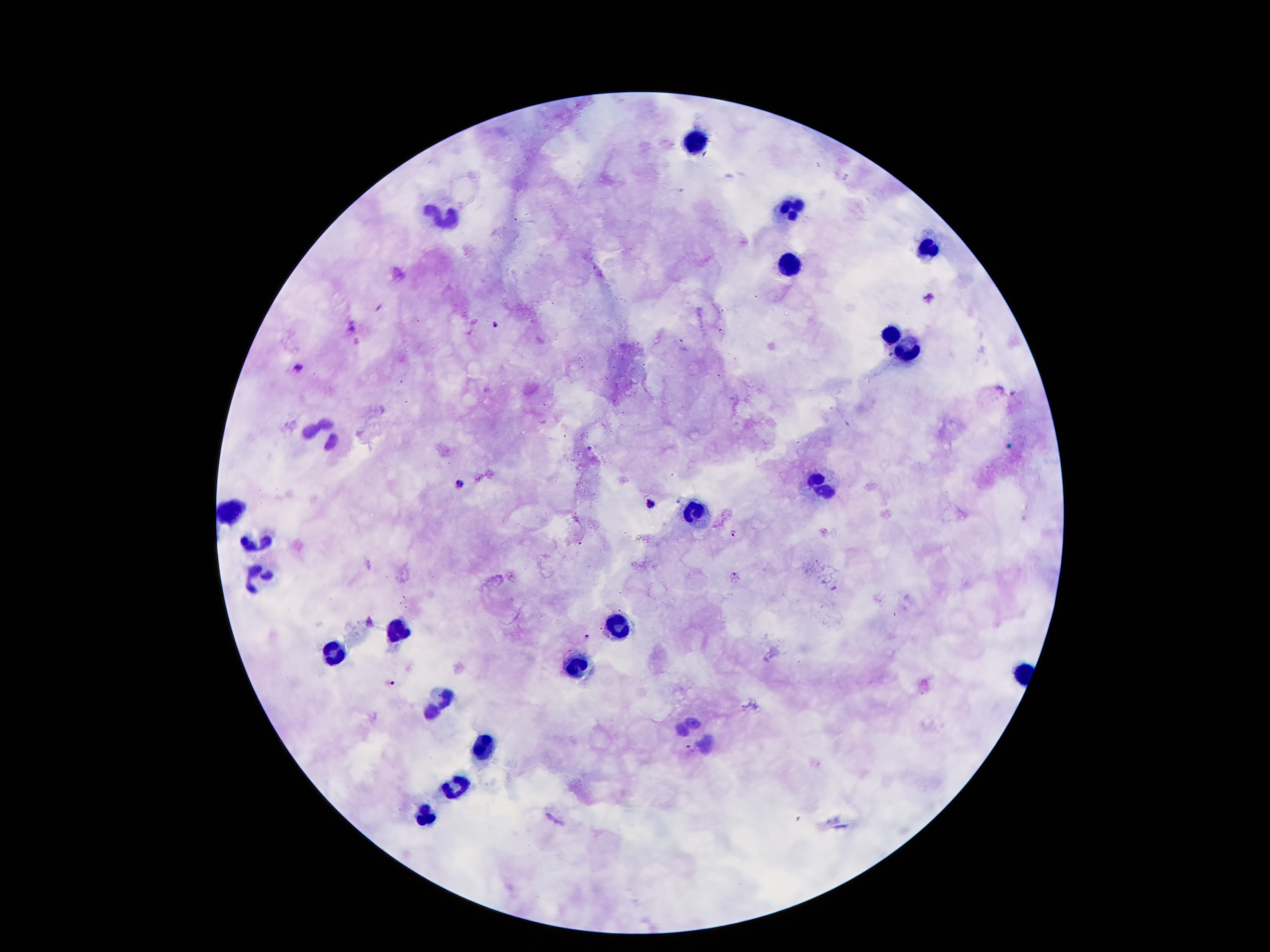 Approximate centers as (x, y) in pixels. Leukocyte locations: (693, 141), (791, 209), (450, 217), (927, 247), (789, 265), (894, 333), (909, 349), (329, 436), (822, 479), (229, 507), (697, 508), (260, 541), (259, 579), (624, 622), (400, 632), (334, 660), (576, 666), (445, 697), (702, 727), (486, 747), (455, 785), (425, 816). Plasmodium parasite locations: (494, 323), (301, 368), (460, 485), (650, 501), (732, 531), (587, 634), (394, 684), (689, 747). Smartphone photograph taken through the microscope eyepiece. Patient malaria status: positive for Plasmodium falciparum. Giemsa stain. Single field of view. 100x magnification. Image is 1270×952 pixels. Thick blood film.